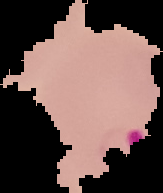
Summary:
  - Result: malaria parasites identified
  - Image type: cell region segmented out of the field of view; surrounding area masked to black
  - Preparation: thin blood smear
  - Image size: 163×193 pixels